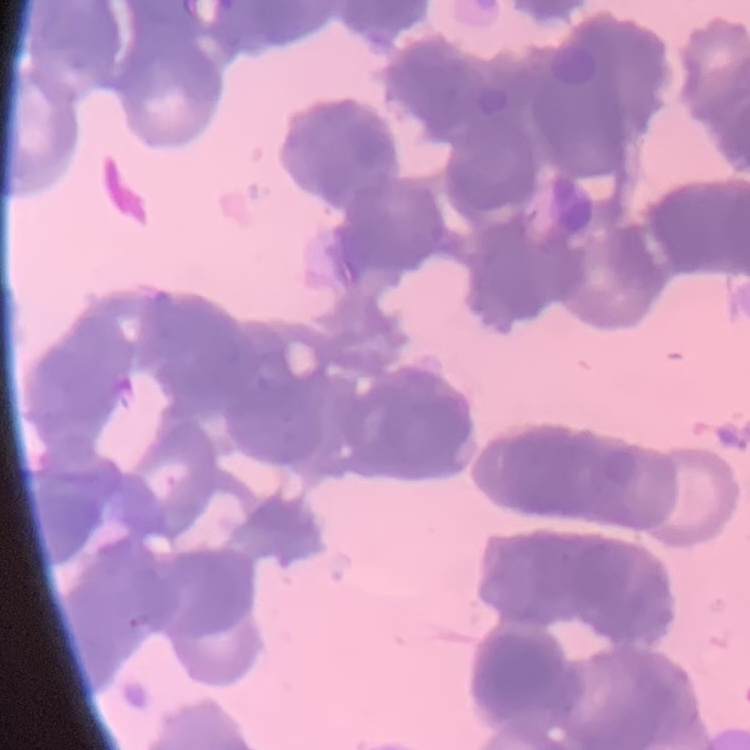

Summary:
  - Red blood cell morphology: rouleaux formation
  - Image type: one tile cut from a larger photomicrograph
  - Preparation: thin blood film
  - Stain: Field's or Giemsa